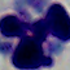

Summary:
  - Magnification: 1000x
  - Identification: white blood cell
  - Modality: micrograph